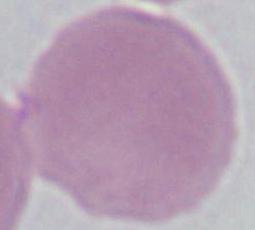

Summary:
  - Magnification: 1000x
  - Identification: erythrocyte
  - Modality: photomicrograph